Outline each blood parasite and name the species.
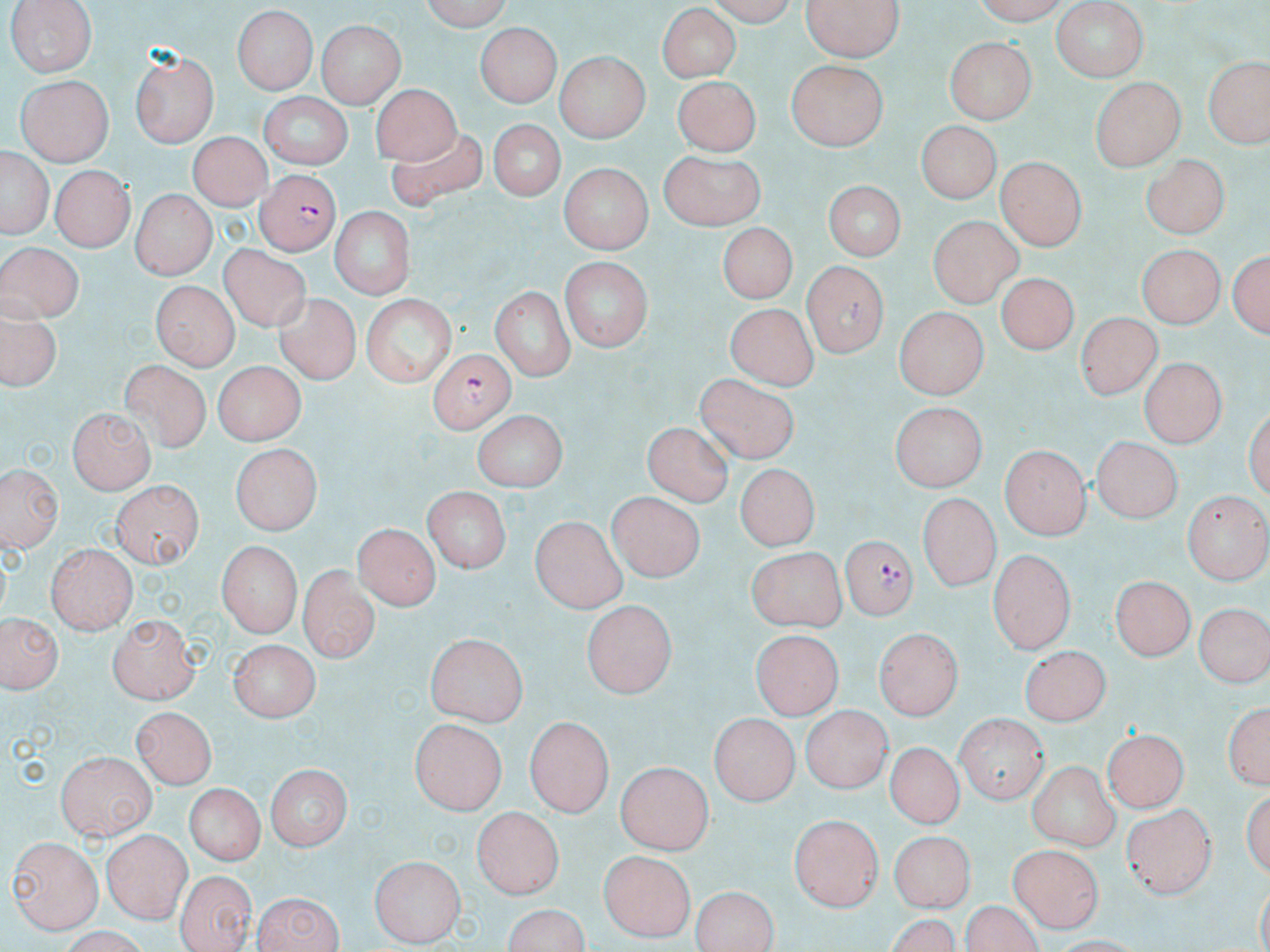

Approximate bounding boxes as (x1,y1)-(x2,y2) corner pairs in pixels.
Plasmodium falciparum-infected red blood cells: (257,172)-(340,254), (429,348)-(512,433), (835,535)-(915,620).
No Plasmodium ovale, Plasmodium malariae, Plasmodium vivax, Babesia divergens, or Trypanosoma brucei observed.

slide_level_diagnosis: Plasmodium falciparum
uninfected_red_blood_cell_locations: 'approximate bounding boxes as (x1,y1)-(x2,y2) corner pairs in pixels: (5,0)-(97,78), (417,0)-(510,29), (699,0)-(801,23), (800,0)-(905,61), (967,0)-(1073,22), (1048,1)-(1148,81), (658,6)-(740,83), (229,8)-(319,96), (315,19)-(405,108), (477,23)-(557,106), (943,37)-(1037,122), (133,49)-(217,148), (556,52)-(650,142), (1206,60)-(1265,147), (788,61)-(885,152), (674,71)-(761,154), (14,74)-(114,167), (1089,75)-(1185,169), (372,84)-(460,168), (257,93)-(350,169), (484,120)-(566,201), (920,122)-(1000,205), (188,129)-(266,210), (387,132)-(485,214), (658,150)-(768,230), (2,151)-(48,239), (1143,154)-(1227,242), (997,156)-(1086,251), (557,165)-(653,252), (49,166)-(134,251), (820,179)-(907,262), (132,190)-(212,279), (328,206)-(415,298), (929,214)-(1021,307), (721,224)-(795,302), (0,238)-(76,321), (220,244)-(311,335), (1137,244)-(1223,329), (1231,247)-(1268,340), (559,260)-(652,352), (802,262)-(887,359), (999,269)-(1080,352), (150,283)-(234,369), (487,284)-(577,380), (362,292)-(456,387), (271,293)-(366,384), (727,303)-(815,389), (893,308)-(988,397), (1077,313)-(1159,402), (0,316)-(61,390), (1137,357)-(1223,449), (120,359)-(209,454), (212,360)-(302,446), (698,371)-(799,465), (887,404)-(988,492), (70,407)-(153,493), (471,411)-(564,491), (644,426)-(732,506), (1088,437)-(1180,523), (228,445)-(324,533), (1002,447)-(1090,540), (735,461)-(821,548), (227,469)-(311,631), (4,473)-(60,549), (111,479)-(203,568), (420,488)-(511,575), (1184,489)-(1269,581), (609,492)-(707,582), (917,493)-(1002,592), (931,512)-(1043,607), (531,518)-(626,614), (352,522)-(439,611), (215,541)-(302,637), (43,542)-(135,633), (744,546)-(847,629), (990,550)-(1076,649), (297,567)-(376,664), (1112,574)-(1194,664), (580,601)-(679,696), (1195,605)-(1267,688), (106,613)-(197,702), (3,614)-(62,698), (875,628)-(964,719), (753,632)-(838,720), (427,634)-(526,725), (231,639)-(321,722), (1021,646)-(1111,724), (1222,695)-(1268,794), (134,706)-(217,790), (800,707)-(891,793), (960,711)-(1048,799), (709,712)-(801,801), (525,716)-(614,817), (412,719)-(505,816), (1103,728)-(1189,809), (59,730)-(195,810), (883,742)-(958,831), (57,750)-(158,839), (1028,760)-(1119,851), (262,762)-(353,852), (617,762)-(713,853), (186,780)-(264,866), (1119,800)-(1215,899), (473,806)-(561,900), (790,814)-(883,914), (892,830)-(971,916), (102,831)-(191,920), (9,834)-(104,933), (1011,843)-(1102,932), (601,849)-(695,942), (371,856)-(462,947), (176,869)-(255,952), (688,886)-(782,950), (250,890)-(347,952), (963,898)-(1044,952), (499,904)-(593,952)'
stain: May-Grünwald-Giemsa
image_size: 1270×952 pixels
magnification: 1000x
preparation: thin blood smear
field_of_view: one of a larger specimen
modality: optical microscopy